Report the malaria status of this cell.
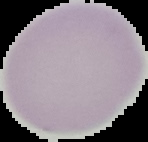

Uninfected.

image_type: cell region segmented out of the field of view; surrounding area masked to black
image_size: 148×142 pixels
preparation: thin blood film